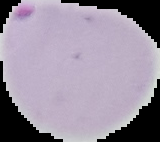

Segmented cell region on a black background. From a thin blood film. Image is 160×142 pixels. Malaria status: parasitized.